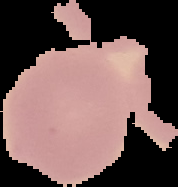

image_size: 178×187 pixels
image_type: cell region segmented out of the field of view; surrounding area masked to black
preparation: thin blood film
malaria_status: uninfected